Classify this cell by malaria status.
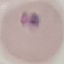
Parasitized.

Summary:
  - Stain: Giemsa
  - Preparation: thin blood smear
  - Image type: cell patch, automatically extracted from a larger field of view and resized to 64 × 64 pixels
  - Capture: smartphone through the microscope eyepiece